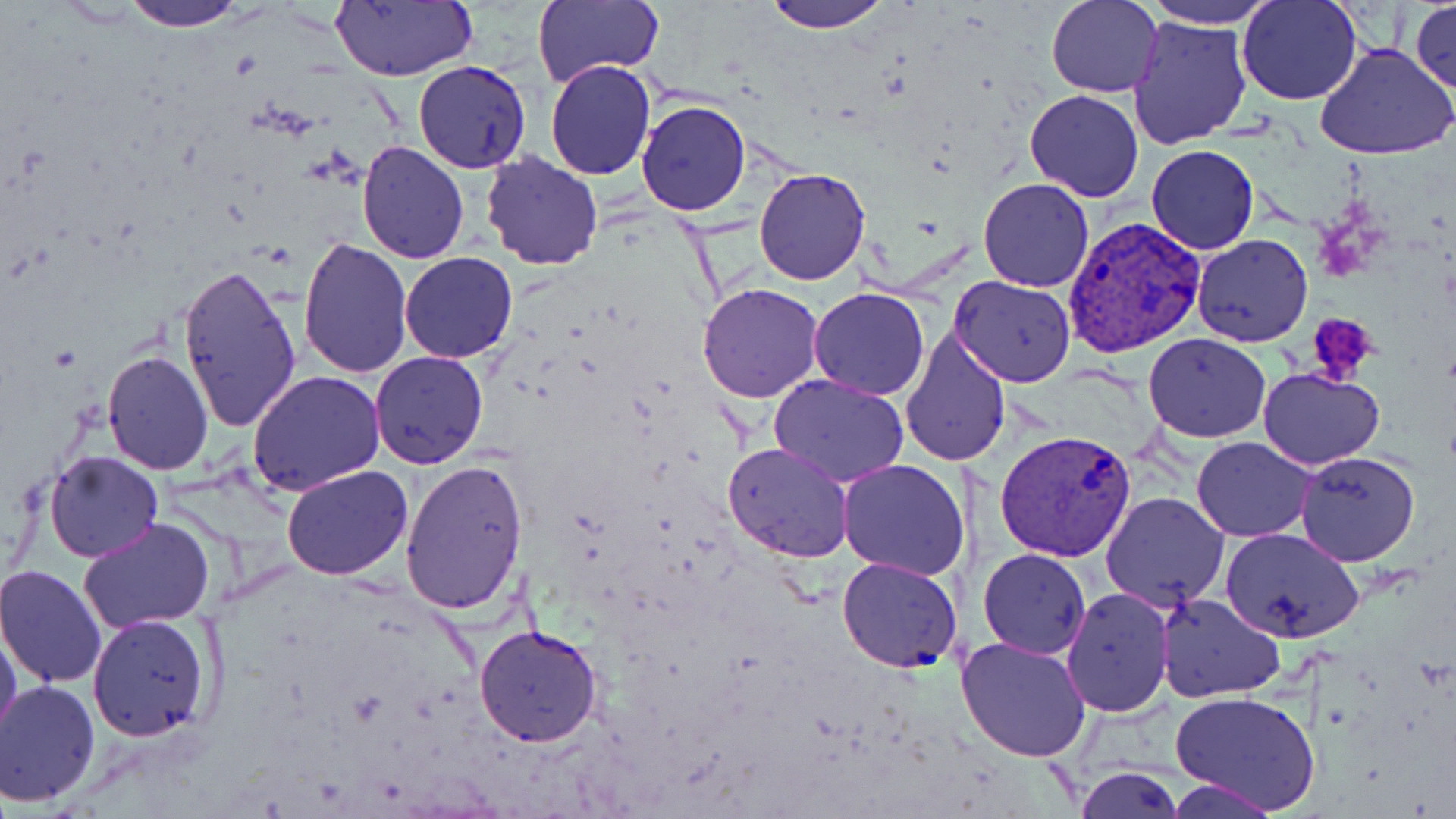

Summary:
  - Coordinate format: approximate bounding boxes as named x1/y1/x2/y2 corners in pixels
  - Platelet locations: (x1=1308, y1=314, x2=1380, y2=383)
  - Plasmodium vivax-infected red blood cell locations: (x1=1061, y1=215, x2=1208, y2=359), (x1=996, y1=428, x2=1136, y2=562)
  - Uninfected red blood cell locations: (x1=120, y1=0, x2=251, y2=30), (x1=327, y1=0, x2=480, y2=83), (x1=532, y1=0, x2=662, y2=89), (x1=763, y1=0, x2=893, y2=31), (x1=1046, y1=0, x2=1163, y2=98), (x1=1141, y1=0, x2=1282, y2=29), (x1=1236, y1=0, x2=1363, y2=107), (x1=1410, y1=2, x2=1455, y2=96), (x1=1127, y1=15, x2=1253, y2=150), (x1=1314, y1=43, x2=1454, y2=161), (x1=545, y1=59, x2=656, y2=180), (x1=413, y1=61, x2=532, y2=173), (x1=1026, y1=89, x2=1143, y2=201), (x1=636, y1=99, x2=751, y2=216), (x1=357, y1=141, x2=470, y2=263), (x1=1147, y1=144, x2=1259, y2=255), (x1=478, y1=151, x2=605, y2=273), (x1=753, y1=167, x2=870, y2=285), (x1=978, y1=178, x2=1094, y2=292), (x1=1191, y1=233, x2=1312, y2=348), (x1=298, y1=238, x2=413, y2=379), (x1=399, y1=252, x2=519, y2=363), (x1=178, y1=260, x2=303, y2=433), (x1=949, y1=276, x2=1076, y2=386), (x1=696, y1=282, x2=824, y2=403), (x1=807, y1=288, x2=929, y2=399), (x1=899, y1=326, x2=1013, y2=467), (x1=1143, y1=332, x2=1272, y2=442), (x1=101, y1=351, x2=214, y2=475), (x1=369, y1=351, x2=488, y2=468), (x1=1258, y1=367, x2=1383, y2=470), (x1=247, y1=371, x2=386, y2=495), (x1=770, y1=374, x2=909, y2=488), (x1=1192, y1=436, x2=1316, y2=541), (x1=722, y1=442, x2=854, y2=564), (x1=1294, y1=450, x2=1421, y2=566), (x1=45, y1=451, x2=163, y2=562), (x1=399, y1=458, x2=529, y2=615), (x1=837, y1=459, x2=969, y2=582), (x1=282, y1=464, x2=413, y2=580), (x1=1101, y1=491, x2=1230, y2=611), (x1=79, y1=516, x2=216, y2=633), (x1=1219, y1=526, x2=1365, y2=644), (x1=978, y1=548, x2=1090, y2=659), (x1=837, y1=557, x2=964, y2=673), (x1=0, y1=566, x2=106, y2=688), (x1=1061, y1=587, x2=1175, y2=716), (x1=1157, y1=593, x2=1287, y2=704), (x1=85, y1=613, x2=216, y2=743), (x1=0, y1=621, x2=22, y2=743), (x1=473, y1=624, x2=603, y2=747), (x1=956, y1=635, x2=1093, y2=762), (x1=0, y1=679, x2=100, y2=806), (x1=1170, y1=691, x2=1322, y2=815), (x1=1075, y1=766, x2=1184, y2=819), (x1=1167, y1=778, x2=1282, y2=818)
  - Slide-level diagnosis: Plasmodium vivax
  - Modality: light microscopy
  - Preparation: thin blood smear
  - Stain: May-Grünwald-Giemsa
  - Magnification: 1000x
  - Image size: 1456×819 pixels
  - Field of view: one of a larger specimen